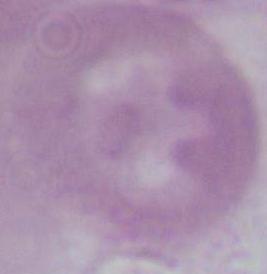
A red blood cell is seen. Photomicrograph. 1000x magnification.